Outline each Plasmodium falciparum-infected red blood cell.
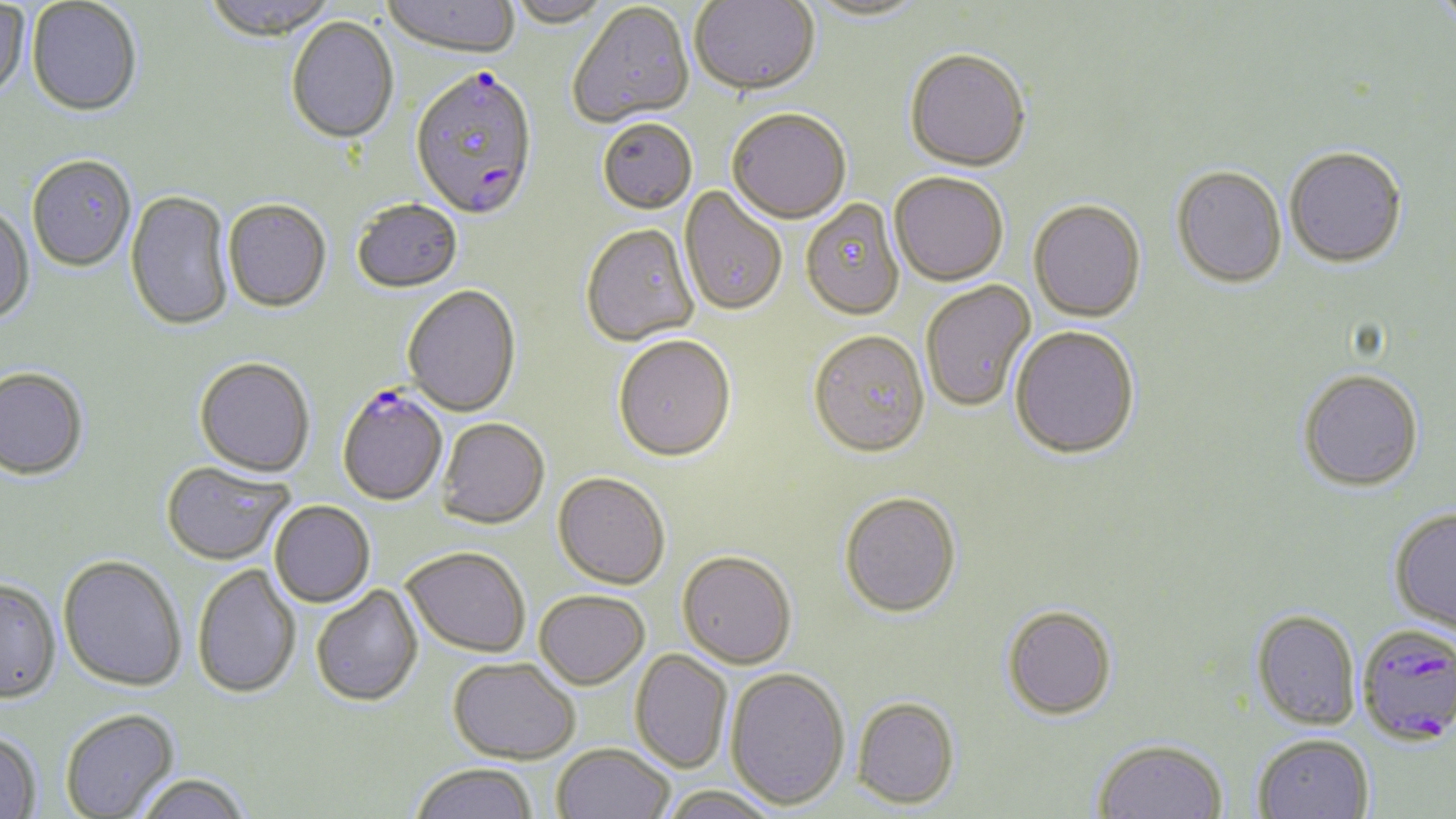
Approximate bounding boxes as (x1,y1)-(x2,y2) corner pairs in pixels.
Plasmodium falciparum-infected red blood cells: (409,70)-(538,223), (337,387)-(449,508), (1356,623)-(1456,746).

slide-level diagnosis = Plasmodium falciparum
stain = May-Grünwald-Giemsa
field of view = single
magnification = 1000x
preparation = thin blood smear
modality = optical microscopy
uninfected red blood cell locations = approximate bounding boxes as (x1,y1)-(x2,y2) corner pairs in pixels: (27,0)-(142,117), (203,0)-(335,45), (381,0)-(520,60), (506,0)-(612,29), (689,0)-(820,98), (804,1)-(929,24), (0,2)-(29,100), (1426,2)-(1456,28), (567,4)-(694,129), (286,18)-(399,146), (904,51)-(1031,173), (727,110)-(851,226), (597,119)-(698,215), (1284,146)-(1407,268), (26,154)-(137,272), (1171,167)-(1287,290), (889,173)-(1008,286), (679,186)-(787,318), (125,190)-(234,332), (800,199)-(905,320), (223,200)-(331,312), (351,200)-(463,294), (1028,201)-(1146,323), (0,204)-(35,326), (580,225)-(699,347), (920,281)-(1036,412), (402,286)-(521,417), (1010,326)-(1140,460), (808,330)-(930,457), (612,336)-(736,463), (194,357)-(315,477), (0,367)-(88,480), (1298,369)-(1424,491), (436,418)-(549,529), (160,460)-(293,565), (553,472)-(671,590), (839,492)-(961,617), (269,501)-(375,607), (1389,507)-(1456,636), (402,547)-(530,658), (677,550)-(796,669), (58,555)-(186,692), (192,564)-(301,699), (0,578)-(61,703), (311,585)-(424,708), (534,590)-(649,689), (1002,604)-(1117,720), (1251,609)-(1361,730), (629,649)-(733,773), (447,657)-(580,764), (725,667)-(850,809), (852,696)-(960,808), (60,708)-(179,818), (0,730)-(42,819), (1252,734)-(1374,819), (1093,739)-(1228,819), (551,744)-(674,819), (410,763)-(538,819), (134,774)-(251,819), (661,784)-(780,819)
image size = 1456×819 pixels